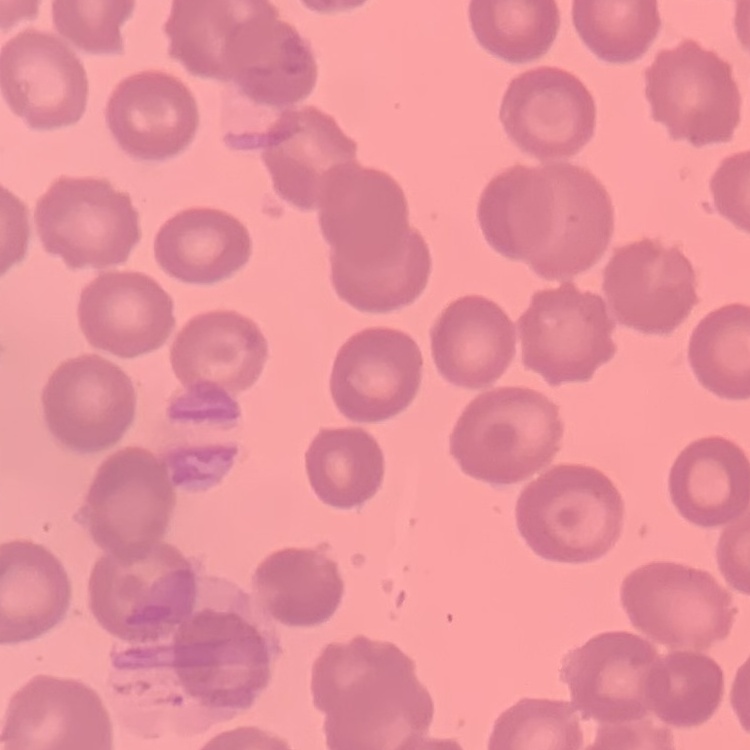

Summary:
  - Red blood cell morphology: no rouleaux formation
  - Image type: square crop of a larger photomicrograph
  - Preparation: thin peripheral smear
  - Stain: Field's or Giemsa